Report the malaria status of this cell.
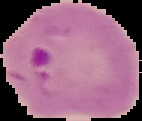
It is parasitized.

From a thin blood film. Image is 142×121 pixels. Cell region segmented out of the field of view; the surrounding area is masked to black.